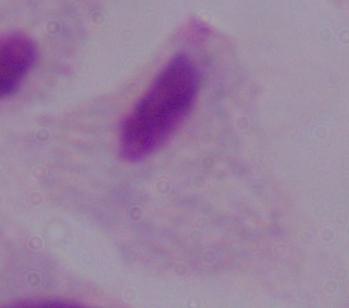
modality = photomicrograph
identification = trichomonad
magnification = 1000x